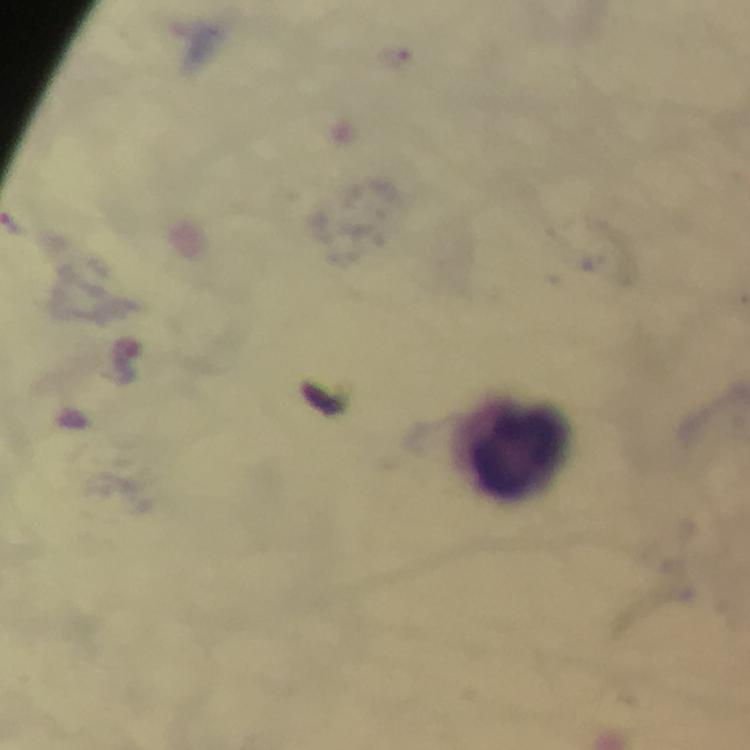 Approximate object centers, in pixels from the top-left corner. Leukocyte locations: (x=519, y=452). Malaria parasite locations: (x=396, y=55). Immersion oil was used. A crop from one field of view. Thick blood smear. From a malaria diagnostic workup. Image is 750×750 pixels. At 100x magnification. Giemsa stain. Photographed with a smartphone mounted on the microscope.